Report the malaria status.
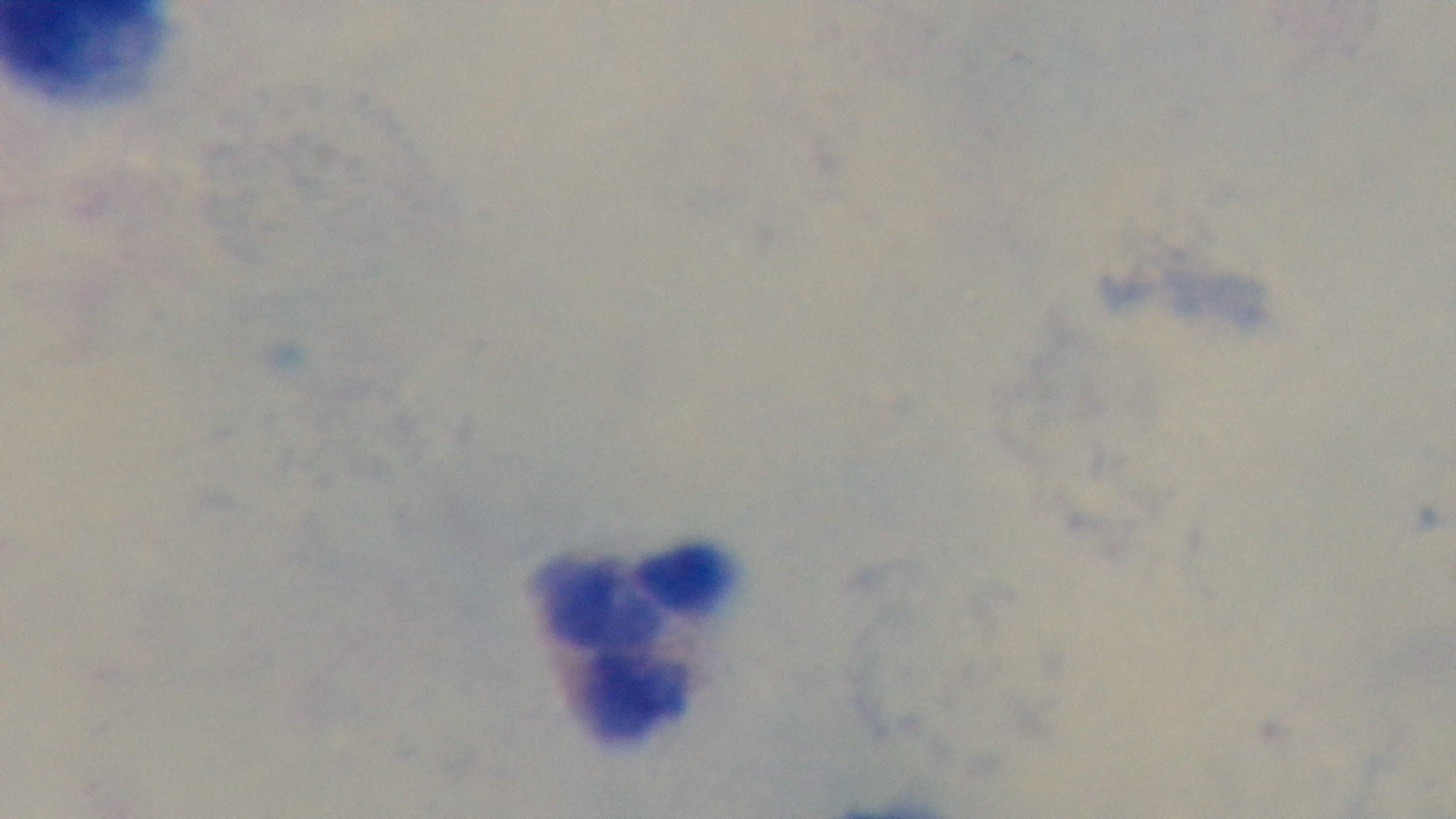

It is uninfected.

Summary:
  - Field of view: single
  - Capture: mounted 4K digital camera
  - Preparation: thick blood film
  - Objective: 100x oil immersion
  - Modality: light microscopy
  - Stain: Giemsa